Identify the blood parasite species.
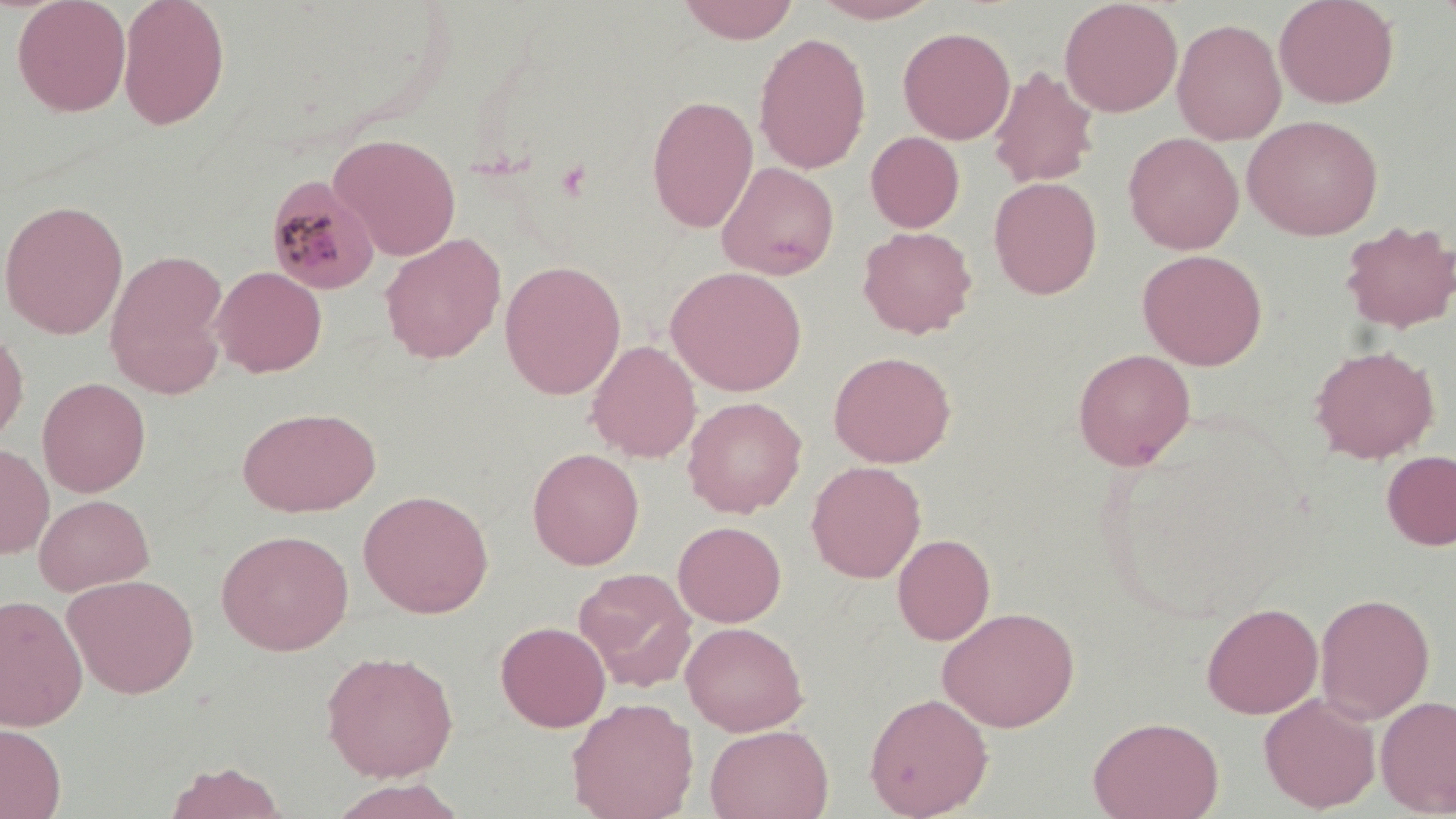

Plasmodium malariae.

Approximate bounding boxes as named x1/y1/x2/y2 corners in pixels. Uninfected red blood cell locations: (x1=12, y1=0, x2=131, y2=117), (x1=117, y1=0, x2=230, y2=130), (x1=675, y1=0, x2=801, y2=44), (x1=809, y1=0, x2=944, y2=23), (x1=1059, y1=0, x2=1183, y2=117), (x1=1273, y1=0, x2=1400, y2=109), (x1=1434, y1=0, x2=1456, y2=31), (x1=1172, y1=18, x2=1287, y2=145), (x1=897, y1=26, x2=1015, y2=144), (x1=753, y1=32, x2=871, y2=175), (x1=988, y1=66, x2=1099, y2=188), (x1=646, y1=95, x2=759, y2=233), (x1=1242, y1=114, x2=1383, y2=240), (x1=866, y1=131, x2=965, y2=233), (x1=1123, y1=132, x2=1244, y2=254), (x1=329, y1=133, x2=462, y2=261), (x1=716, y1=161, x2=839, y2=280), (x1=988, y1=177, x2=1103, y2=299), (x1=0, y1=199, x2=129, y2=339), (x1=1338, y1=219, x2=1455, y2=333), (x1=858, y1=225, x2=977, y2=338), (x1=380, y1=233, x2=506, y2=364), (x1=1136, y1=248, x2=1268, y2=370), (x1=105, y1=249, x2=230, y2=398), (x1=499, y1=260, x2=626, y2=400), (x1=211, y1=266, x2=327, y2=377), (x1=665, y1=266, x2=807, y2=396), (x1=0, y1=322, x2=29, y2=448), (x1=587, y1=340, x2=701, y2=462), (x1=1310, y1=344, x2=1440, y2=463), (x1=1072, y1=348, x2=1195, y2=471), (x1=828, y1=350, x2=956, y2=468), (x1=37, y1=377, x2=151, y2=497), (x1=682, y1=396, x2=806, y2=518), (x1=238, y1=406, x2=380, y2=517), (x1=0, y1=442, x2=54, y2=559), (x1=527, y1=447, x2=645, y2=570), (x1=1381, y1=451, x2=1456, y2=550), (x1=806, y1=461, x2=926, y2=583), (x1=358, y1=489, x2=494, y2=618), (x1=34, y1=493, x2=154, y2=596), (x1=46, y1=493, x2=178, y2=674), (x1=673, y1=520, x2=786, y2=627), (x1=216, y1=529, x2=354, y2=655), (x1=892, y1=533, x2=995, y2=645), (x1=573, y1=567, x2=697, y2=691), (x1=62, y1=573, x2=199, y2=699), (x1=1314, y1=591, x2=1435, y2=723), (x1=0, y1=593, x2=88, y2=731), (x1=1201, y1=602, x2=1323, y2=719), (x1=936, y1=606, x2=1080, y2=731), (x1=495, y1=620, x2=611, y2=732), (x1=681, y1=621, x2=808, y2=736), (x1=321, y1=650, x2=459, y2=781), (x1=863, y1=692, x2=994, y2=818), (x1=1259, y1=693, x2=1381, y2=813), (x1=1376, y1=695, x2=1456, y2=816), (x1=566, y1=697, x2=698, y2=819), (x1=1088, y1=715, x2=1224, y2=819), (x1=0, y1=723, x2=66, y2=819), (x1=705, y1=724, x2=834, y2=819), (x1=164, y1=761, x2=287, y2=819), (x1=326, y1=779, x2=469, y2=819). Plasmodium malariae-infected red blood cell locations: (x1=264, y1=174, x2=383, y2=294). Image is 1456×819 pixels. Single field of view. Thin blood film. May-Grünwald-Giemsa stain. 1000x magnification. Light microscopy.